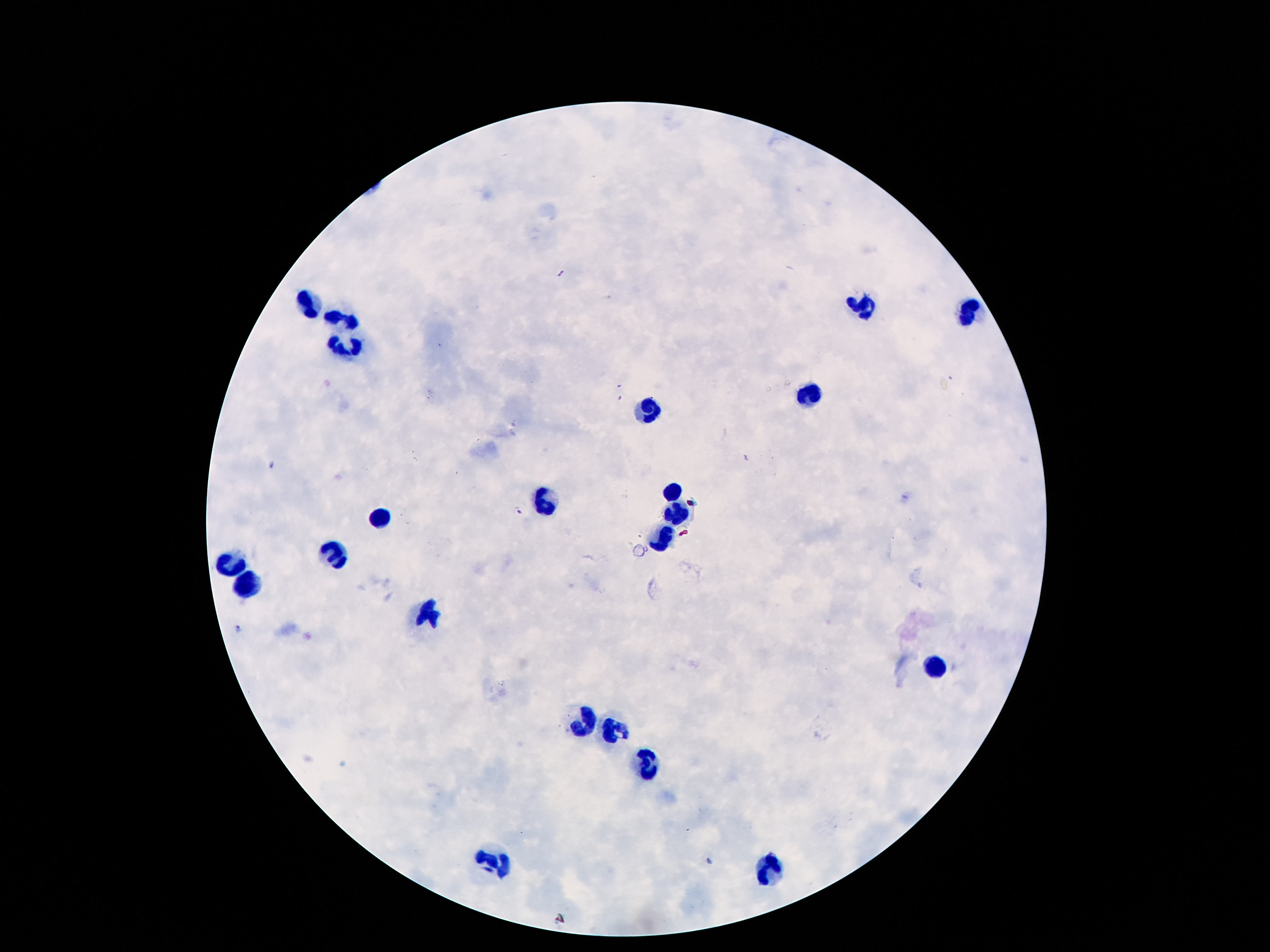

{
  "preparation": "thick peripheral-blood smear",
  "patient_malaria_status": "not infected",
  "stain": "Giemsa",
  "field_of_view": "one from this slide",
  "leukocyte_locations": "approximate centers as [x, y] in pixels: [306, 300], [862, 305], [967, 309], [339, 317], [348, 344], [808, 394], [652, 408], [675, 490], [542, 501], [675, 512], [379, 513], [666, 536], [334, 559], [227, 564], [246, 585], [428, 613], [940, 666], [580, 722], [610, 728], [648, 765], [767, 862], [493, 863]",
  "capture": "smartphone camera through the microscope eyepiece",
  "image_size": "1270×952 pixels",
  "magnification": "100x"
}